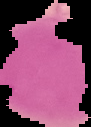

Summary:
  - Preparation: thin blood smear
  - Image size: 91×127 pixels
  - Malaria status: uninfected
  - Image type: cell region segmented out of the field of view; surrounding area masked to black